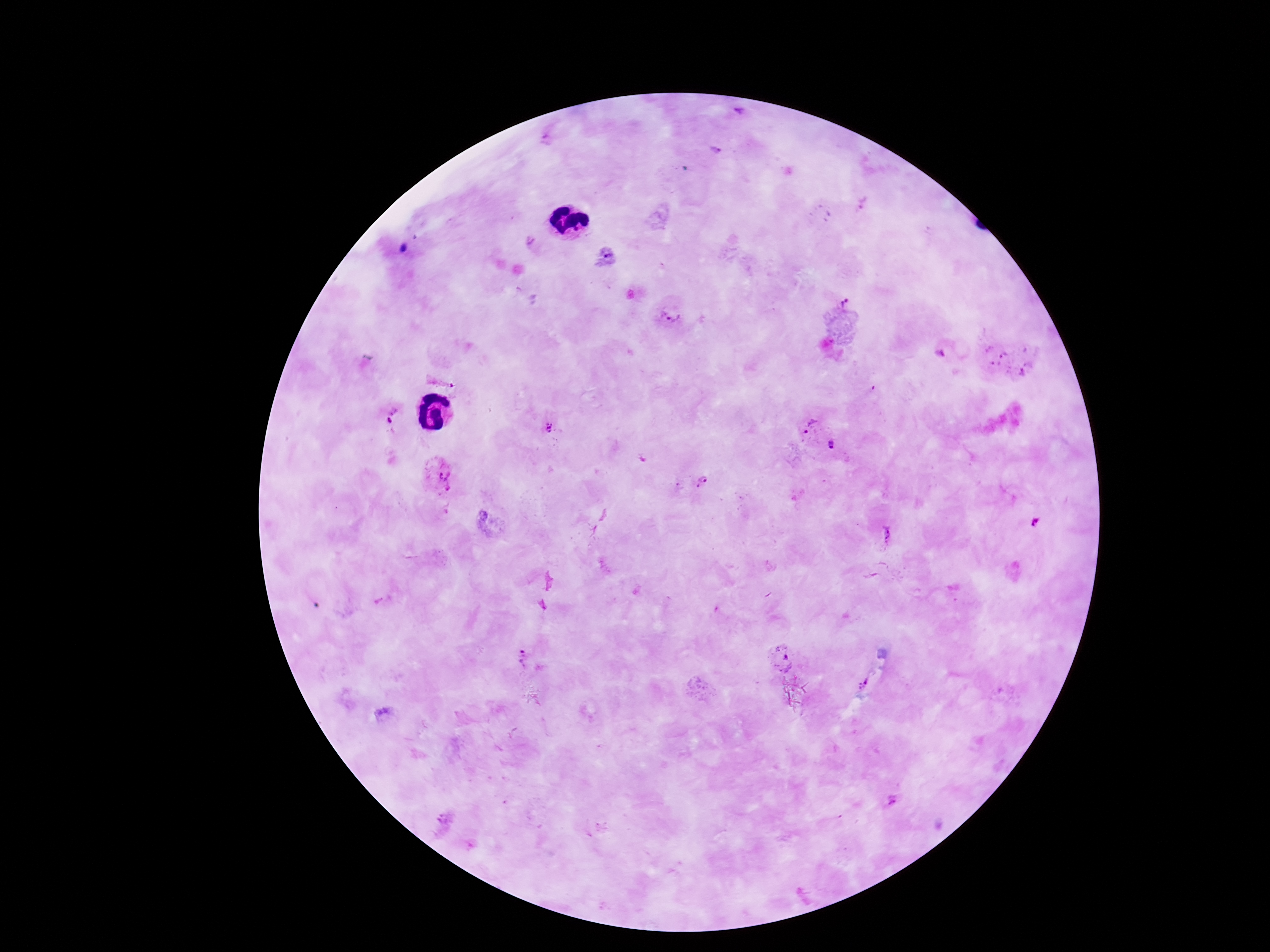

Approximate object centers, in pixels from the top-left corner.
Summary:
  - Plasmodium parasite locations: (x=740, y=115), (x=863, y=207), (x=842, y=302), (x=672, y=313), (x=941, y=352), (x=1007, y=359), (x=442, y=378), (x=388, y=415), (x=810, y=427), (x=549, y=428), (x=836, y=444), (x=439, y=477), (x=703, y=482), (x=1034, y=521), (x=889, y=535), (x=784, y=657), (x=523, y=662), (x=865, y=685), (x=894, y=801)
  - Patient malaria status: positive
  - Stain: Giemsa
  - Magnification: 100x
  - Capture: smartphone camera through the microscope eyepiece
  - Field of view: single
  - Preparation: thick blood film
  - Image size: 1270×952 pixels